State which cell type is depicted.
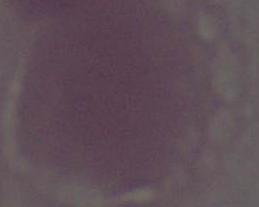
This is an erythrocyte.

Micrograph. 1000x magnification.